Identify the parasite.
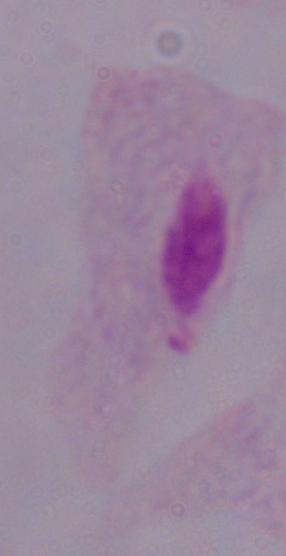

This is a trichomonad.

Summary:
  - Modality: photomicrograph
  - Magnification: 1000x